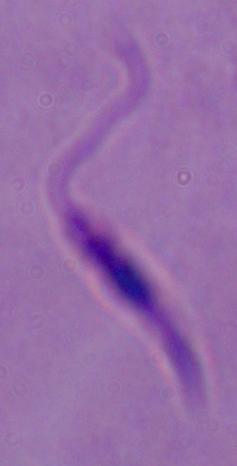
Summary:
  - Magnification: 1000x
  - Identification: Leishmania
  - Modality: photomicrograph